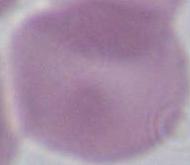
magnification = 1000x
identification = red blood cell
modality = photomicrograph